State which parasite is depicted.
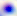
This is Toxoplasma gondii.

Summary:
  - Magnification: 400x
  - Modality: photomicrograph